Name the parasite shown.
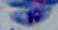
Toxoplasma gondii.

magnification = 1000x
modality = photomicrograph